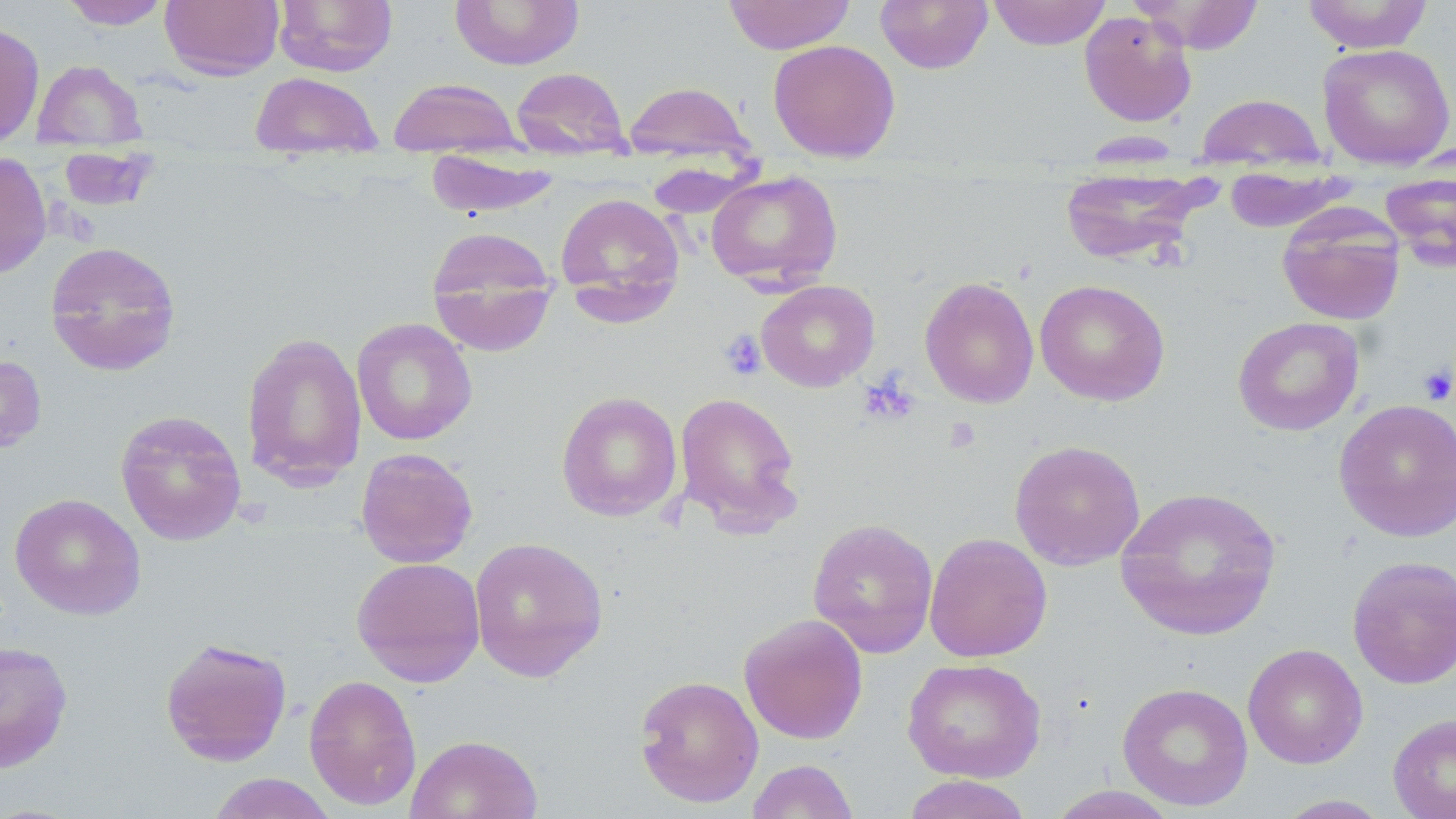

slide-level diagnosis = negative for blood parasites
magnification = 1000x
modality = light microscopy
stain = May-Grünwald-Giemsa
platelet locations = approximate bounding boxes as [x1, y1, x2, y2] in pixels: [718, 329, 767, 381], [1417, 364, 1456, 405], [859, 375, 920, 426], [943, 416, 981, 454]
uninfected red blood cell locations = approximate bounding boxes as [x1, y1, x2, y2] in pixels: [59, 0, 172, 29], [160, 0, 284, 80], [273, 0, 398, 76], [449, 0, 584, 70], [722, 0, 856, 55], [875, 0, 994, 74], [988, 0, 1111, 50], [1129, 0, 1265, 54], [1301, 0, 1433, 53], [1079, 11, 1197, 127], [0, 22, 45, 148], [767, 39, 901, 163], [1317, 43, 1456, 170], [32, 59, 146, 149], [511, 67, 631, 160], [250, 71, 382, 158], [388, 77, 522, 157], [622, 81, 754, 166], [1195, 93, 1327, 173], [58, 147, 157, 214], [425, 151, 562, 218], [0, 152, 52, 280], [1223, 166, 1355, 233], [1058, 167, 1213, 267], [1380, 169, 1456, 272], [706, 171, 843, 289], [555, 192, 685, 312], [1277, 205, 1406, 326], [425, 226, 559, 357], [44, 240, 182, 377], [919, 276, 1039, 408], [1034, 279, 1171, 406], [756, 280, 880, 391], [1232, 316, 1364, 436], [351, 317, 477, 445], [240, 332, 367, 490], [0, 353, 47, 454], [556, 390, 683, 522], [674, 391, 804, 535], [1333, 398, 1456, 541], [114, 409, 247, 546], [1008, 439, 1146, 570], [356, 447, 479, 568], [1114, 485, 1283, 641], [9, 493, 146, 621], [807, 517, 939, 658], [924, 532, 1053, 662], [469, 536, 609, 683], [1347, 555, 1456, 689], [350, 556, 486, 687], [738, 613, 869, 744], [159, 636, 292, 766], [0, 641, 74, 772], [1243, 643, 1368, 769], [902, 658, 1046, 782], [303, 673, 421, 811], [634, 674, 764, 807], [1117, 681, 1254, 811], [1387, 712, 1456, 819], [405, 734, 543, 819], [745, 759, 860, 818], [206, 772, 339, 819], [901, 774, 1034, 819], [1045, 785, 1183, 819], [1274, 795, 1393, 818]
image size = 1456×819 pixels
field of view = one of a larger specimen
preparation = thin blood smear